Classify this cell by malaria status.
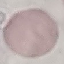
It is uninfected.

Summary:
  - Preparation: thin smear
  - Image type: cell patch, automatically extracted from a larger field of view and resized to 64 × 64 pixels
  - Capture: smartphone through the microscope eyepiece
  - Stain: Giemsa